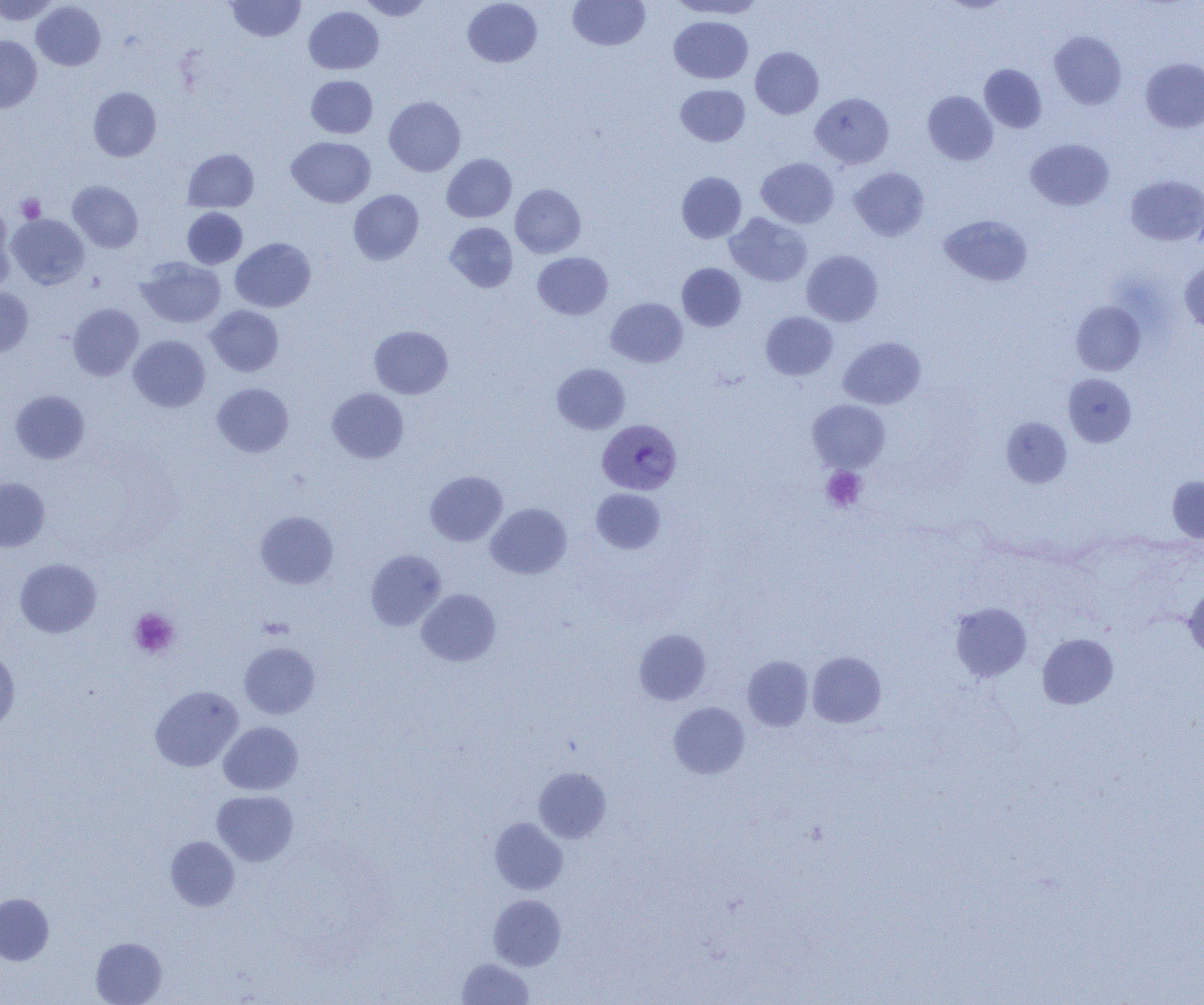
{
  "slide_level_diagnosis": "Plasmodium vivax",
  "image_size": "1204×1005 pixels",
  "plasmodium_vivax_infected_red_blood_cell_locations": "approximate bounding boxes as named x1/y1/x2/y2 corners in pixels: (x1=597, y1=419, x2=681, y2=495)",
  "uninfected_red_blood_cell_locations": "approximate bounding boxes as named x1/y1/x2/y2 corners in pixels: (x1=0, y1=0, x2=59, y2=25), (x1=225, y1=0, x2=305, y2=41), (x1=359, y1=0, x2=433, y2=20), (x1=463, y1=0, x2=542, y2=67), (x1=568, y1=0, x2=650, y2=51), (x1=669, y1=0, x2=766, y2=19), (x1=940, y1=0, x2=1012, y2=13), (x1=31, y1=1, x2=105, y2=70), (x1=304, y1=6, x2=384, y2=74), (x1=669, y1=15, x2=752, y2=84), (x1=1049, y1=31, x2=1127, y2=109), (x1=0, y1=35, x2=42, y2=112), (x1=750, y1=47, x2=823, y2=118), (x1=1141, y1=58, x2=1204, y2=133), (x1=979, y1=64, x2=1047, y2=133), (x1=306, y1=75, x2=378, y2=138), (x1=675, y1=84, x2=750, y2=146), (x1=88, y1=87, x2=161, y2=161), (x1=923, y1=91, x2=998, y2=165), (x1=810, y1=92, x2=894, y2=168), (x1=384, y1=96, x2=465, y2=176), (x1=286, y1=136, x2=375, y2=207), (x1=1026, y1=139, x2=1114, y2=211), (x1=183, y1=149, x2=259, y2=212), (x1=441, y1=154, x2=516, y2=222), (x1=756, y1=157, x2=838, y2=228), (x1=849, y1=167, x2=929, y2=241), (x1=676, y1=171, x2=747, y2=243), (x1=1125, y1=175, x2=1204, y2=246), (x1=68, y1=181, x2=143, y2=252), (x1=510, y1=184, x2=586, y2=258), (x1=348, y1=189, x2=423, y2=265), (x1=0, y1=206, x2=15, y2=293), (x1=182, y1=208, x2=247, y2=269), (x1=724, y1=212, x2=812, y2=286), (x1=7, y1=214, x2=89, y2=289), (x1=939, y1=214, x2=1033, y2=287), (x1=444, y1=222, x2=518, y2=292), (x1=231, y1=237, x2=316, y2=312), (x1=801, y1=250, x2=883, y2=326), (x1=532, y1=252, x2=613, y2=320), (x1=137, y1=257, x2=226, y2=328), (x1=1180, y1=262, x2=1204, y2=335), (x1=677, y1=263, x2=747, y2=331), (x1=0, y1=287, x2=33, y2=356), (x1=606, y1=298, x2=688, y2=368), (x1=1071, y1=301, x2=1145, y2=375), (x1=68, y1=303, x2=143, y2=380), (x1=206, y1=305, x2=283, y2=376), (x1=761, y1=311, x2=838, y2=380), (x1=369, y1=326, x2=453, y2=398), (x1=129, y1=335, x2=210, y2=412), (x1=838, y1=336, x2=926, y2=409), (x1=552, y1=363, x2=630, y2=434), (x1=1062, y1=373, x2=1137, y2=447), (x1=212, y1=383, x2=294, y2=457), (x1=327, y1=388, x2=409, y2=463), (x1=10, y1=390, x2=89, y2=464), (x1=807, y1=399, x2=890, y2=472), (x1=1001, y1=417, x2=1071, y2=487), (x1=425, y1=471, x2=508, y2=546), (x1=1167, y1=475, x2=1204, y2=542), (x1=0, y1=478, x2=50, y2=552), (x1=591, y1=488, x2=666, y2=554), (x1=486, y1=503, x2=572, y2=579), (x1=256, y1=511, x2=338, y2=588), (x1=366, y1=549, x2=446, y2=630), (x1=15, y1=558, x2=101, y2=637), (x1=1184, y1=585, x2=1204, y2=660), (x1=416, y1=588, x2=501, y2=666), (x1=950, y1=602, x2=1032, y2=682), (x1=634, y1=629, x2=711, y2=705), (x1=1037, y1=633, x2=1118, y2=709), (x1=239, y1=642, x2=320, y2=718), (x1=0, y1=651, x2=20, y2=729), (x1=807, y1=651, x2=886, y2=728), (x1=742, y1=655, x2=814, y2=731), (x1=150, y1=685, x2=244, y2=772), (x1=669, y1=702, x2=749, y2=779), (x1=218, y1=722, x2=302, y2=795), (x1=534, y1=767, x2=611, y2=843), (x1=212, y1=790, x2=298, y2=866), (x1=490, y1=818, x2=568, y2=894), (x1=165, y1=836, x2=240, y2=911), (x1=0, y1=893, x2=54, y2=965), (x1=488, y1=894, x2=566, y2=970), (x1=91, y1=937, x2=167, y2=1005), (x1=457, y1=958, x2=533, y2=1004)",
  "modality": "optical microscopy",
  "magnification": "1000x",
  "platelet_locations": "approximate bounding boxes as named x1/y1/x2/y2 corners in pixels: (x1=16, y1=194, x2=46, y2=223), (x1=821, y1=466, x2=867, y2=512), (x1=129, y1=608, x2=180, y2=658)",
  "preparation": "thin blood film",
  "field_of_view": "single"
}